Assess the morphology of the red blood cells.
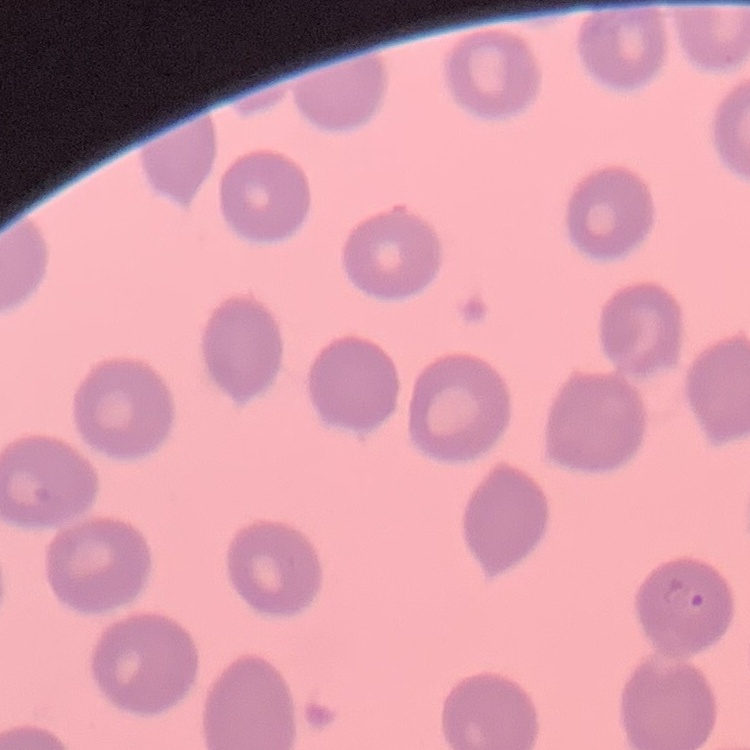
No rouleaux formation.

Thin peripheral smear. Stained with either Field's or Giemsa. Square crop of a larger photomicrograph.